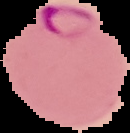

Summary:
  - Malaria status: parasitized
  - Image size: 130×133 pixels
  - Preparation: thin blood smear
  - Image type: segmented cell region on a black background